State which parasite is depicted.
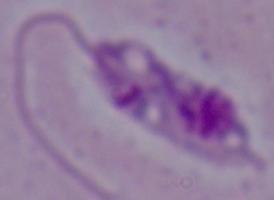
This is Leishmania.

Micrograph. 1000x magnification.